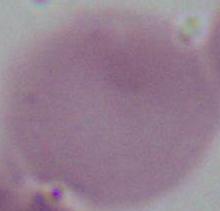

An erythrocyte is shown. Captured at 1000x magnification. Micrograph.